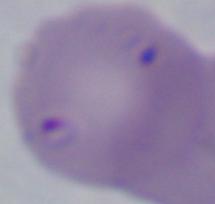 Photomicrograph. A Babesia parasite is seen. Captured at 1000x magnification.